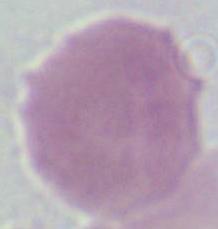

Summary:
  - Modality: micrograph
  - Magnification: 1000x
  - Identification: red blood cell